Report the malaria status of this cell.
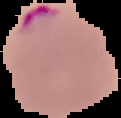

It is parasitized.

preparation = thin blood smear
image type = segmented cell region on a black background
image size = 121×118 pixels